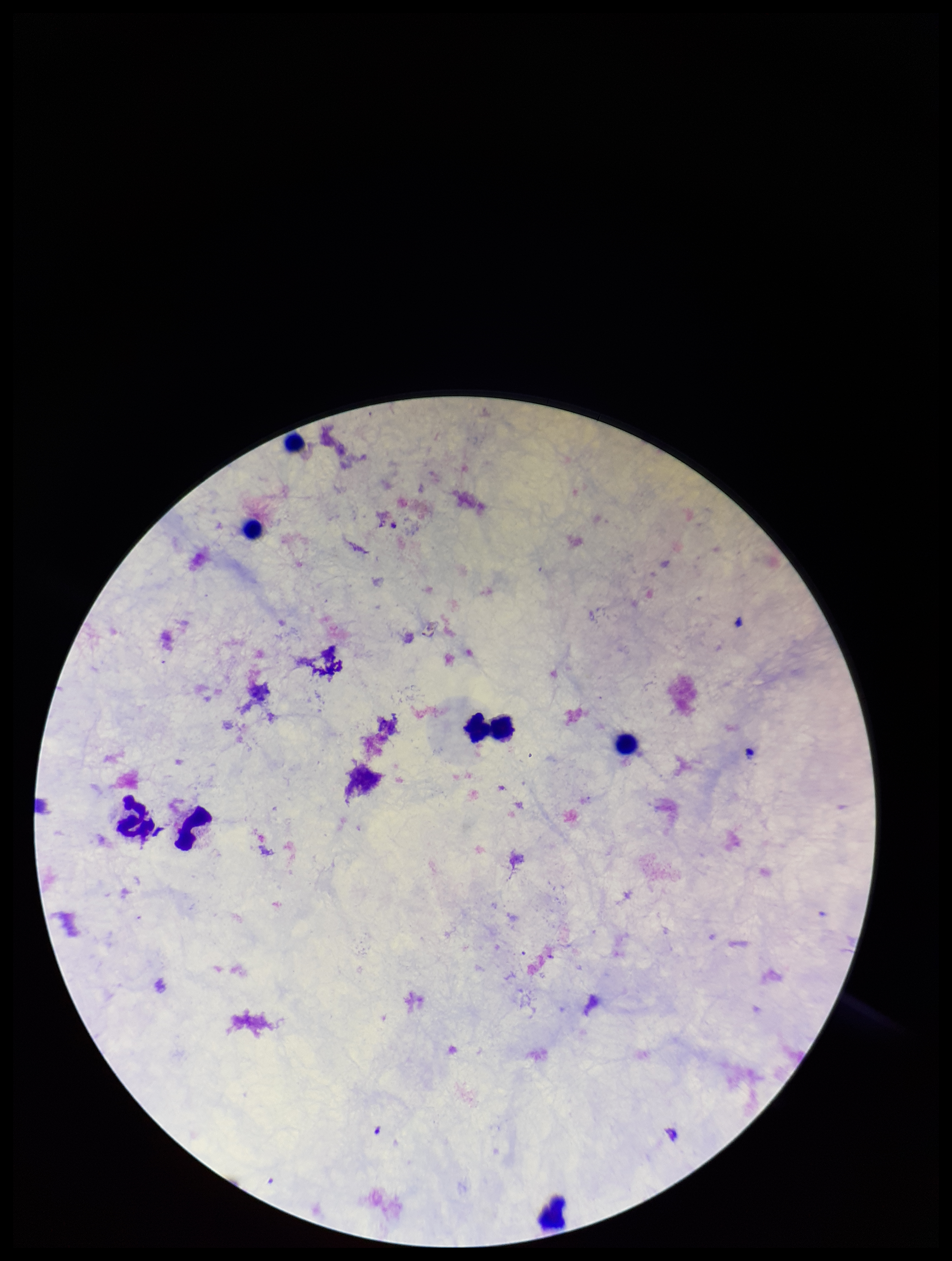
{
  "plasmodium_parasites": "none seen",
  "image_size": "952×1261 pixels",
  "parasite_count": 0,
  "patient_malaria_status": "negative",
  "field_of_view": "one from this slide",
  "leukocyte_count": 8,
  "preparation": "thick blood smear",
  "stain": "Giemsa",
  "capture": "smartphone photograph through the microscope eyepiece"
}